Assess this cell for malaria.
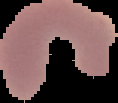

Parasitized.

image type = segmented cell region on a black background
image size = 118×103 pixels
preparation = thin blood smear